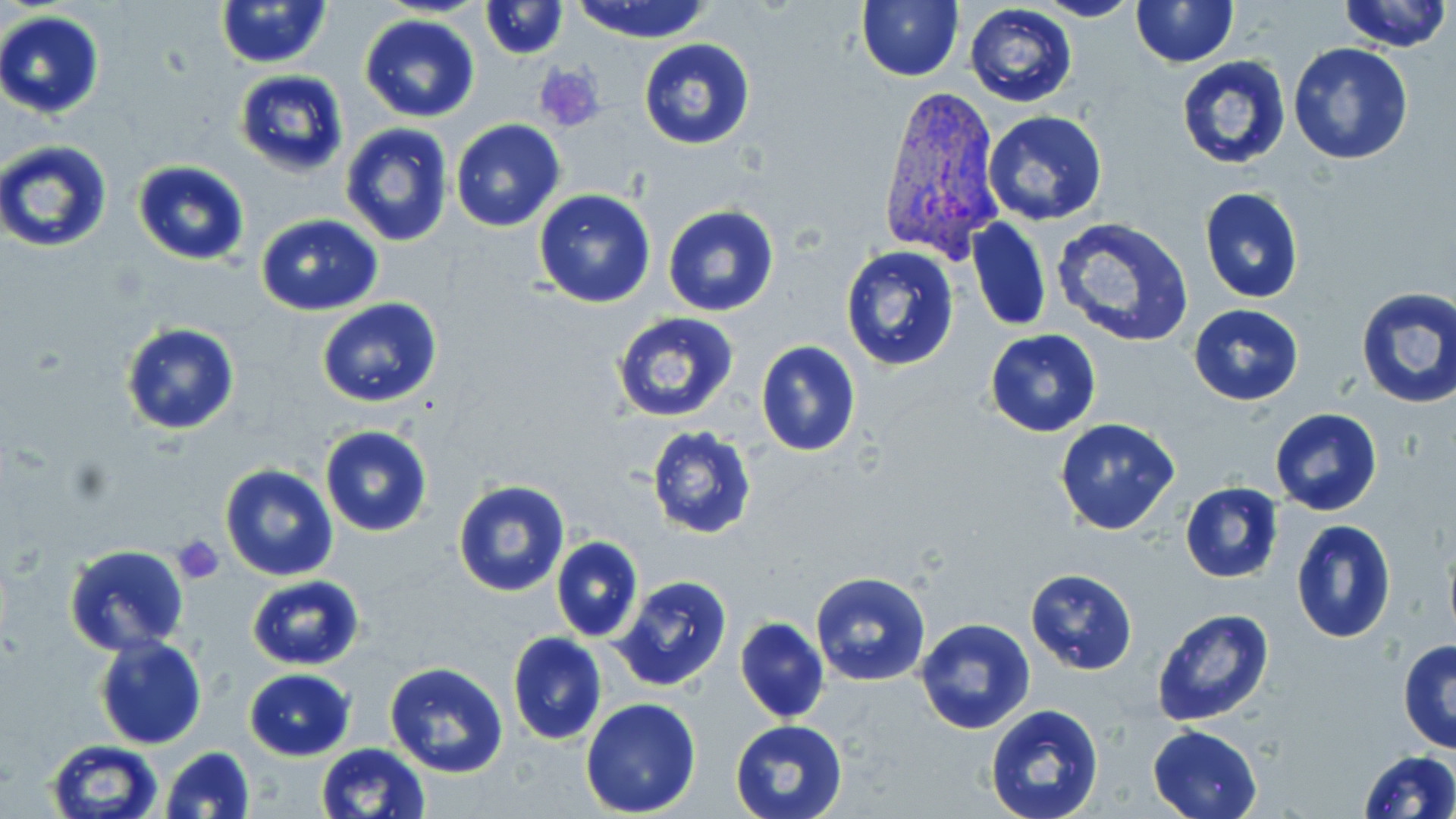

Approximate bounding boxes as [x1, y1, x2, y2] in pixels. Platelet locations: [533, 64, 606, 134], [170, 535, 225, 584]. Uninfected red blood cell locations: [214, 0, 331, 69], [481, 0, 566, 58], [569, 0, 715, 44], [856, 0, 964, 83], [1032, 0, 1141, 22], [1131, 0, 1238, 68], [1339, 0, 1453, 53], [965, 4, 1077, 108], [0, 11, 105, 118], [359, 15, 481, 123], [638, 38, 755, 151], [1287, 43, 1414, 166], [1175, 55, 1291, 171], [235, 70, 349, 179], [984, 110, 1108, 225], [450, 120, 565, 232], [339, 123, 453, 249], [1, 140, 113, 253], [132, 161, 251, 265], [1199, 187, 1304, 304], [533, 190, 656, 308], [662, 205, 780, 317], [256, 215, 383, 315], [969, 217, 1053, 333], [1050, 217, 1194, 348], [840, 246, 960, 371], [1355, 286, 1456, 409], [317, 298, 442, 408], [1189, 304, 1303, 404], [612, 310, 741, 424], [120, 323, 241, 436], [985, 329, 1101, 438], [755, 340, 861, 457], [1268, 407, 1383, 515], [1054, 417, 1181, 535], [645, 425, 759, 540], [319, 426, 433, 537], [220, 464, 338, 583], [452, 479, 570, 597], [1180, 482, 1284, 583], [1289, 518, 1397, 644], [551, 538, 642, 641], [64, 545, 190, 657], [1024, 568, 1139, 675], [809, 572, 932, 687], [611, 574, 735, 693], [246, 575, 365, 670], [1150, 607, 1275, 728], [735, 617, 829, 723], [914, 618, 1037, 737], [508, 633, 607, 745], [95, 634, 207, 750], [1398, 640, 1456, 754], [384, 662, 509, 780], [243, 669, 355, 761], [579, 698, 702, 818], [984, 705, 1107, 819], [729, 717, 849, 819], [1149, 724, 1264, 819], [46, 741, 162, 819], [316, 743, 429, 819], [161, 746, 255, 818], [1357, 750, 1456, 819]. Plasmodium vivax-infected red blood cell locations: [875, 86, 1003, 263]. Slide-level diagnosis: Plasmodium vivax. May-Grünwald-Giemsa stain. Optical microscopy. Thin blood film. Single field of view. Captured at 1000x magnification. Image is 1456×819 pixels.